Locate every blood parasite and identify its species.
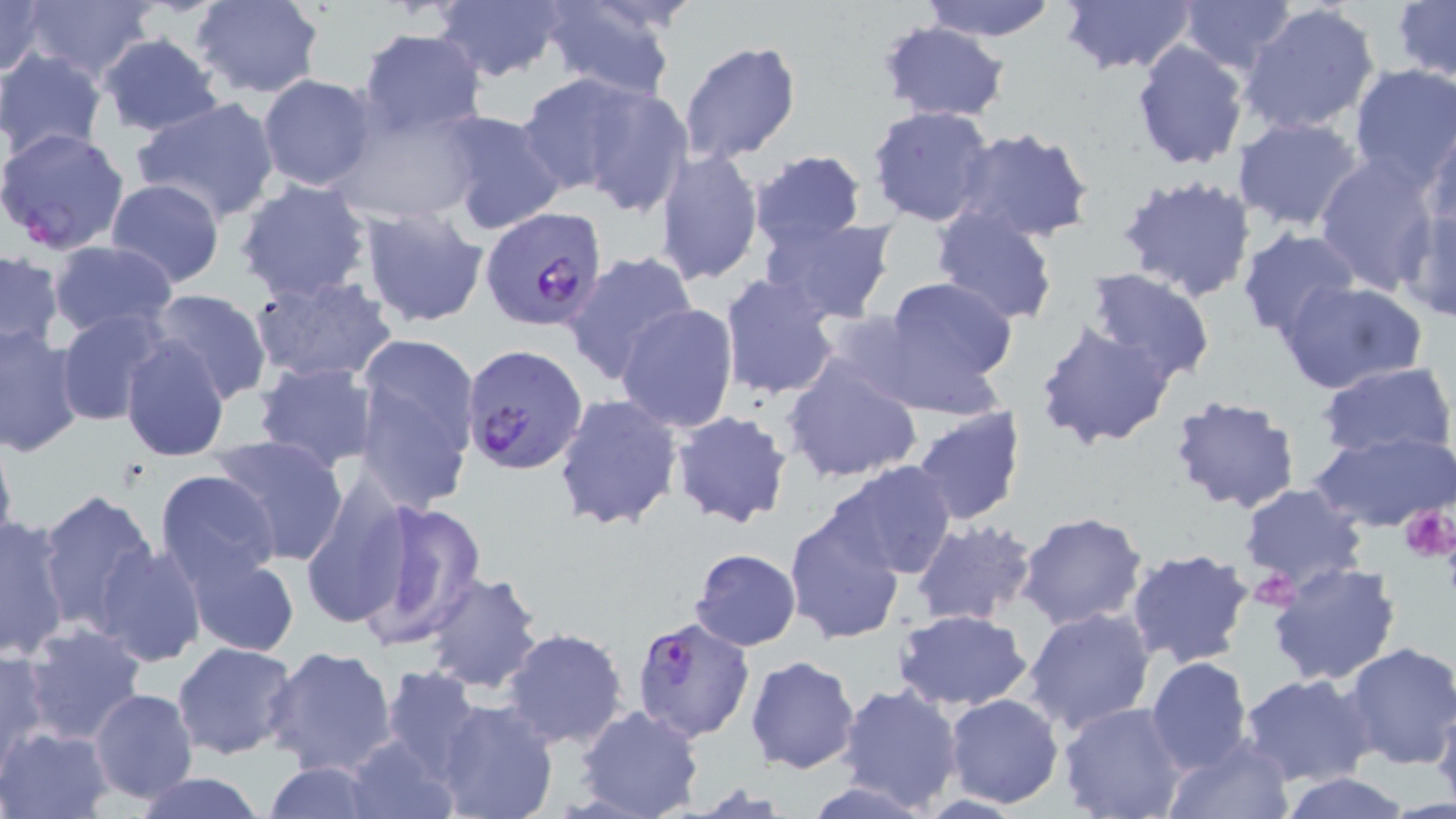

Approximate bounding boxes as named x1/y1/x2/y2 corners in pixels.
Plasmodium falciparum-infected red blood cells: (x1=0, y1=127, x2=132, y2=256), (x1=480, y1=209, x2=610, y2=334), (x1=461, y1=344, x2=588, y2=473), (x1=627, y1=617, x2=757, y2=747).
No Plasmodium ovale, Plasmodium malariae, Plasmodium vivax, Babesia divergens, or Trypanosoma brucei observed.

slide-level diagnosis = Plasmodium falciparum
magnification = 1000x
uninfected red blood cell locations = approximate bounding boxes as named x1/y1/x2/y2 corners in pixels: (x1=431, y1=0, x2=568, y2=83), (x1=1059, y1=0, x2=1197, y2=74), (x1=1177, y1=0, x2=1297, y2=75), (x1=0, y1=1, x2=49, y2=80), (x1=188, y1=1, x2=325, y2=100), (x1=918, y1=1, x2=1063, y2=43), (x1=1394, y1=1, x2=1455, y2=84), (x1=19, y1=2, x2=157, y2=85), (x1=537, y1=2, x2=680, y2=98), (x1=1239, y1=2, x2=1381, y2=136), (x1=878, y1=21, x2=1010, y2=123), (x1=357, y1=28, x2=489, y2=139), (x1=95, y1=34, x2=224, y2=136), (x1=1130, y1=39, x2=1250, y2=172), (x1=677, y1=41, x2=802, y2=165), (x1=0, y1=49, x2=106, y2=162), (x1=1349, y1=64, x2=1456, y2=188), (x1=516, y1=71, x2=653, y2=196), (x1=257, y1=73, x2=376, y2=191), (x1=571, y1=82, x2=695, y2=217), (x1=130, y1=96, x2=282, y2=226), (x1=334, y1=104, x2=486, y2=225), (x1=867, y1=105, x2=996, y2=227), (x1=436, y1=109, x2=567, y2=237), (x1=1231, y1=116, x2=1365, y2=233), (x1=1424, y1=121, x2=1456, y2=238), (x1=951, y1=126, x2=1094, y2=243), (x1=655, y1=149, x2=764, y2=286), (x1=750, y1=149, x2=867, y2=254), (x1=1315, y1=154, x2=1439, y2=293), (x1=1115, y1=177, x2=1258, y2=308), (x1=104, y1=179, x2=225, y2=289), (x1=234, y1=179, x2=374, y2=304), (x1=1398, y1=201, x2=1456, y2=324), (x1=930, y1=202, x2=1060, y2=328), (x1=356, y1=205, x2=489, y2=328), (x1=760, y1=216, x2=896, y2=324), (x1=1235, y1=227, x2=1363, y2=344), (x1=50, y1=239, x2=178, y2=340), (x1=1, y1=249, x2=66, y2=357), (x1=562, y1=250, x2=699, y2=384), (x1=1086, y1=269, x2=1215, y2=384), (x1=246, y1=272, x2=397, y2=385), (x1=718, y1=273, x2=841, y2=400), (x1=876, y1=276, x2=1017, y2=401), (x1=1276, y1=279, x2=1427, y2=393), (x1=148, y1=287, x2=272, y2=404), (x1=616, y1=304, x2=740, y2=434), (x1=55, y1=308, x2=175, y2=427), (x1=1035, y1=321, x2=1178, y2=451), (x1=0, y1=324, x2=85, y2=460), (x1=353, y1=336, x2=480, y2=509), (x1=118, y1=338, x2=229, y2=460), (x1=782, y1=355, x2=924, y2=484), (x1=251, y1=361, x2=382, y2=473), (x1=1317, y1=361, x2=1453, y2=458), (x1=552, y1=393, x2=683, y2=533), (x1=1168, y1=393, x2=1299, y2=515), (x1=909, y1=405, x2=1026, y2=526), (x1=669, y1=409, x2=795, y2=529), (x1=0, y1=426, x2=18, y2=563), (x1=1307, y1=430, x2=1456, y2=533), (x1=208, y1=435, x2=350, y2=565), (x1=830, y1=461, x2=957, y2=579), (x1=154, y1=468, x2=281, y2=588), (x1=298, y1=477, x2=413, y2=631), (x1=1238, y1=483, x2=1369, y2=586), (x1=37, y1=491, x2=162, y2=634), (x1=350, y1=500, x2=489, y2=651), (x1=784, y1=507, x2=906, y2=645), (x1=1016, y1=510, x2=1149, y2=628), (x1=0, y1=514, x2=73, y2=659), (x1=911, y1=520, x2=1038, y2=629), (x1=91, y1=540, x2=208, y2=668), (x1=1125, y1=547, x2=1256, y2=667), (x1=179, y1=548, x2=302, y2=658), (x1=689, y1=548, x2=800, y2=650), (x1=1267, y1=561, x2=1403, y2=688), (x1=420, y1=572, x2=546, y2=693), (x1=1022, y1=606, x2=1156, y2=737), (x1=892, y1=608, x2=1035, y2=712), (x1=20, y1=623, x2=148, y2=747), (x1=502, y1=627, x2=629, y2=749), (x1=171, y1=640, x2=299, y2=759), (x1=1340, y1=641, x2=1456, y2=771), (x1=264, y1=645, x2=399, y2=779), (x1=0, y1=647, x2=51, y2=771), (x1=746, y1=655, x2=861, y2=774), (x1=1145, y1=656, x2=1255, y2=775), (x1=743, y1=665, x2=958, y2=791), (x1=378, y1=666, x2=486, y2=780), (x1=1238, y1=673, x2=1376, y2=789), (x1=836, y1=683, x2=964, y2=814), (x1=88, y1=687, x2=199, y2=806), (x1=944, y1=693, x2=1065, y2=809), (x1=1432, y1=694, x2=1456, y2=809), (x1=432, y1=699, x2=559, y2=819), (x1=1056, y1=701, x2=1189, y2=819), (x1=576, y1=706, x2=704, y2=818), (x1=2, y1=725, x2=111, y2=818), (x1=339, y1=732, x2=458, y2=819), (x1=1163, y1=738, x2=1294, y2=819), (x1=261, y1=762, x2=379, y2=817), (x1=128, y1=772, x2=275, y2=818), (x1=1277, y1=773, x2=1414, y2=818)
field of view = one of a larger specimen
preparation = thin blood smear
stain = May-Grünwald-Giemsa
platelet locations = approximate bounding boxes as named x1/y1/x2/y2 corners in pixels: (x1=1401, y1=503, x2=1456, y2=563)
image size = 1456×819 pixels
modality = optical microscopy